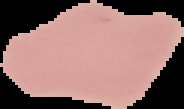
{
  "result": "no malaria parasites seen",
  "image_type": "segmented cell region with the area outside set to black",
  "image_size": "184×109 pixels",
  "preparation": "thin blood smear"
}